Identify the preparation type.
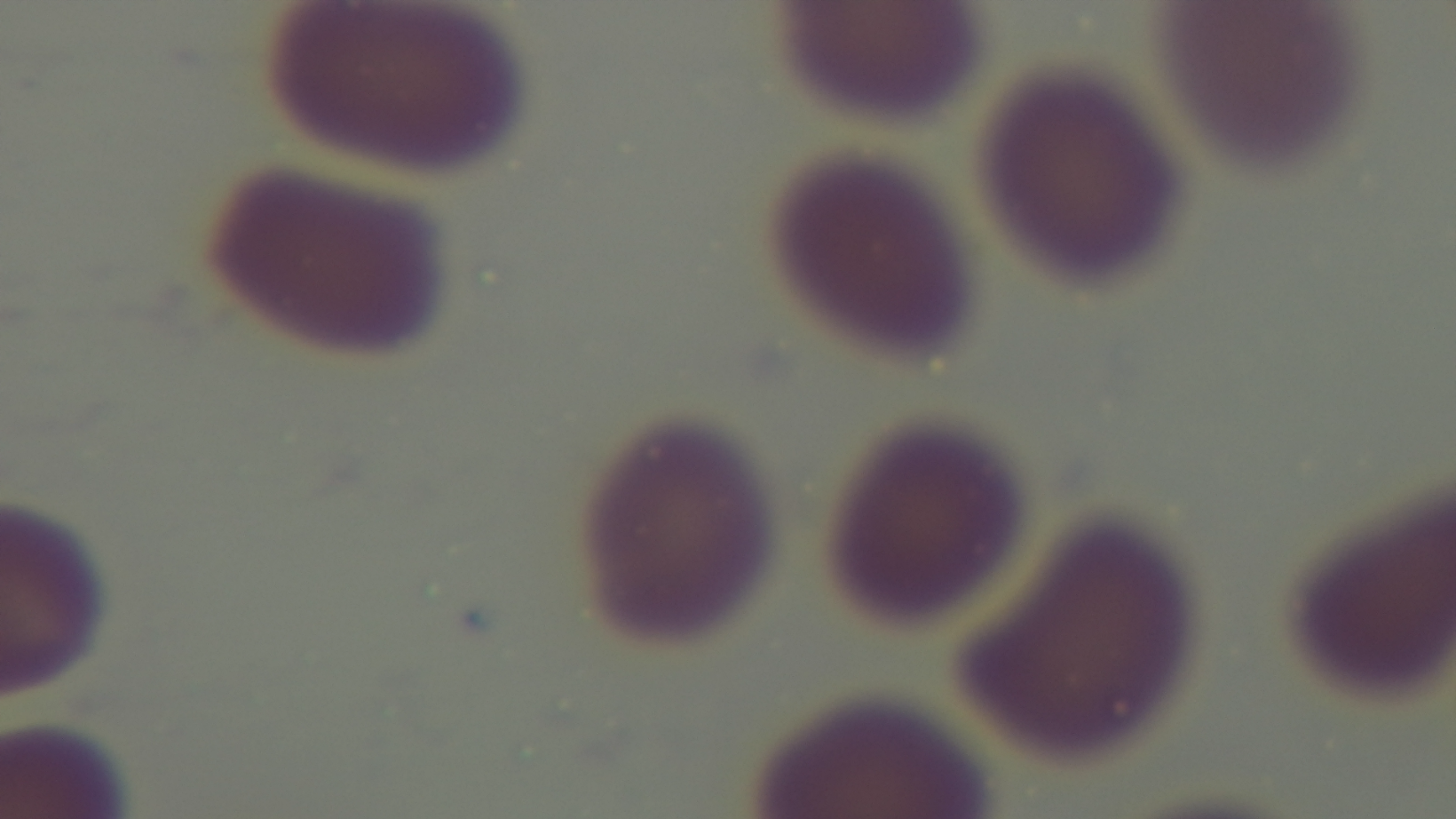
Thin.

modality = light microscopy
malaria status = negative
capture = mounted 4K digital camera
field of view = one from the slide
stain = Giemsa
objective = 100x oil immersion